Classify this cell by malaria status.
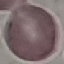
Uninfected.

Photographed with a smartphone camera at the microscope eyepiece. Thin blood smear. Giemsa stain. Automatically extracted cell patch, resized to 64 × 64 pixels.